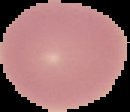

From a thin blood smear. Result: no Plasmodium parasites detected. Cell region segmented out of the field of view; the surrounding area is masked to black. Image is 130×112 pixels.